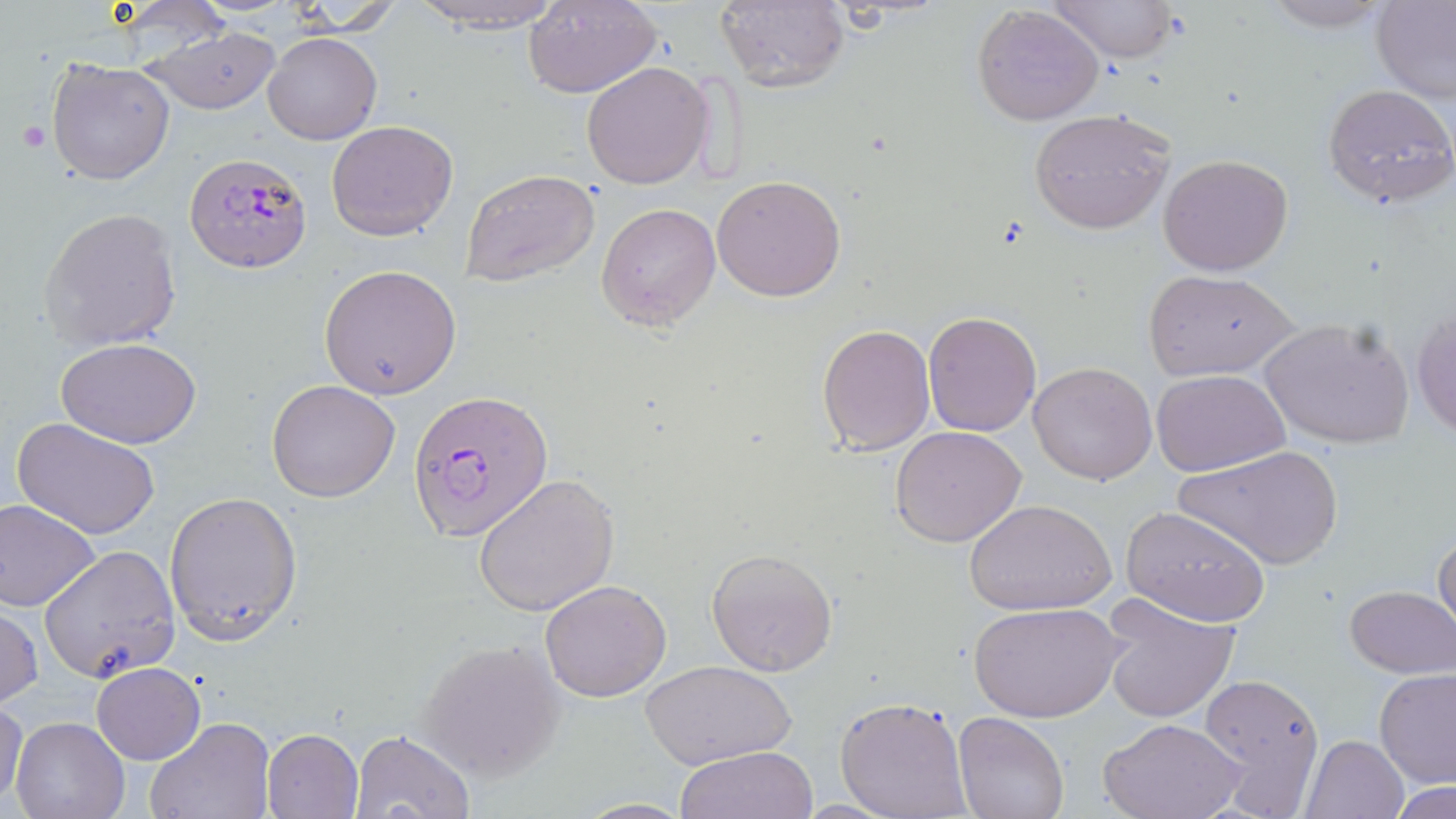

Summary:
  - Coordinate format: approximate bounding boxes as (x1, y1, x2, y2) in pixels
  - Plasmodium falciparum-infected red blood cell locations: (183, 151, 314, 273), (408, 389, 553, 543)
  - Uninfected red blood cell locations: (404, 0, 569, 33), (523, 0, 662, 99), (1048, 0, 1178, 62), (1258, 0, 1396, 32), (714, 1, 849, 92), (1372, 1, 1456, 103), (284, 3, 406, 36), (973, 5, 1105, 125), (146, 28, 282, 115), (263, 29, 382, 145), (47, 59, 174, 185), (580, 62, 714, 190), (1323, 83, 1456, 208), (1029, 107, 1177, 235), (326, 120, 459, 241), (1156, 153, 1295, 275), (460, 169, 601, 288), (711, 173, 846, 302), (596, 202, 722, 330), (40, 206, 184, 350), (319, 264, 462, 400), (1145, 270, 1298, 381), (1411, 302, 1456, 442), (922, 309, 1042, 436), (1257, 316, 1413, 450), (816, 323, 936, 456), (57, 337, 202, 449), (1027, 361, 1158, 485), (1152, 369, 1290, 476), (266, 379, 401, 502), (11, 417, 160, 540), (891, 426, 1028, 548), (1178, 445, 1344, 571), (475, 475, 618, 617), (163, 490, 303, 645), (0, 499, 101, 612), (963, 499, 1116, 615), (1120, 504, 1271, 626), (1433, 528, 1456, 639), (38, 544, 181, 684), (705, 548, 838, 677), (539, 579, 673, 702), (1346, 584, 1455, 678), (1099, 592, 1241, 724), (0, 602, 42, 709), (970, 602, 1125, 722), (417, 638, 567, 782), (642, 659, 796, 771), (92, 663, 204, 764), (1373, 669, 1456, 790), (1196, 671, 1325, 815), (832, 696, 973, 819), (1, 700, 27, 808), (953, 712, 1070, 819), (10, 716, 128, 819), (1100, 716, 1247, 819), (146, 717, 275, 819), (262, 728, 363, 817), (347, 728, 475, 818), (1302, 734, 1410, 819), (675, 746, 820, 819), (1391, 781, 1453, 819), (572, 798, 695, 817)
  - Platelet locations: (13, 118, 53, 155)
  - Slide-level diagnosis: Plasmodium falciparum
  - Magnification: 1000x
  - Modality: light microscopy
  - Field of view: one of a larger specimen
  - Stain: May-Grünwald-Giemsa
  - Image size: 1456×819 pixels
  - Preparation: thin blood smear